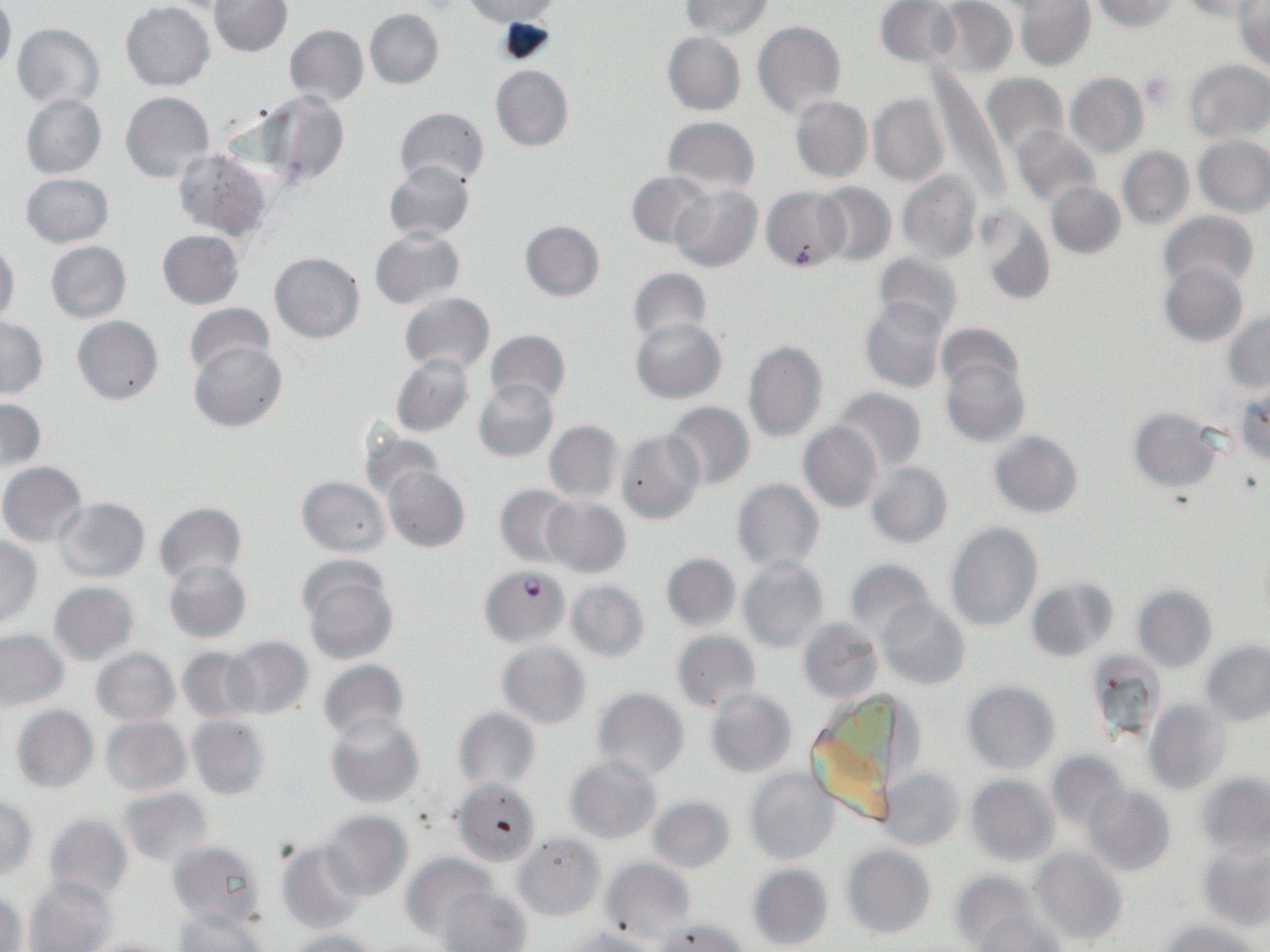
Approximate bounding boxes as [x1, y1, x2, y2] in pixels. Plasmodium falciparum-infected red blood cell locations: [481, 564, 568, 645]. Platelet locations: [1140, 72, 1174, 109]. Uninfected red blood cell locations: [0, 0, 15, 73], [931, 0, 1016, 79], [1090, 0, 1177, 32], [211, 1, 291, 57], [465, 1, 561, 24], [681, 1, 771, 39], [875, 1, 960, 67], [1017, 1, 1094, 69], [1178, 1, 1259, 20], [1233, 2, 1270, 70], [122, 3, 214, 90], [365, 8, 444, 89], [753, 19, 845, 120], [12, 24, 106, 108], [284, 25, 368, 106], [662, 32, 745, 115], [1184, 60, 1269, 142], [490, 65, 573, 152], [929, 67, 1001, 196], [983, 73, 1067, 160], [1066, 73, 1148, 158], [120, 91, 214, 182], [260, 92, 348, 186], [21, 93, 106, 179], [869, 93, 949, 186], [790, 96, 871, 182], [393, 107, 489, 190], [662, 117, 759, 195], [1010, 126, 1099, 208], [1194, 137, 1270, 216], [1121, 142, 1265, 219], [1118, 147, 1193, 229], [172, 149, 274, 241], [383, 160, 474, 244], [31, 170, 122, 325], [898, 170, 983, 264], [626, 171, 711, 251], [20, 174, 113, 247], [812, 182, 896, 267], [1047, 182, 1125, 258], [670, 186, 762, 272], [762, 186, 848, 272], [977, 208, 1053, 306], [1158, 212, 1258, 291], [519, 220, 605, 302], [370, 229, 464, 311], [158, 230, 244, 310], [0, 241, 20, 326], [45, 241, 132, 323], [270, 252, 364, 343], [873, 253, 963, 336], [1160, 261, 1247, 346], [628, 268, 711, 345], [400, 292, 494, 375], [860, 299, 947, 393], [185, 303, 275, 379], [1223, 313, 1270, 393], [72, 316, 164, 404], [631, 317, 726, 403], [0, 319, 48, 397], [936, 322, 1023, 397], [485, 329, 570, 410], [742, 339, 828, 442], [189, 342, 287, 433], [391, 353, 474, 437], [941, 358, 1029, 448], [473, 378, 558, 462], [1233, 384, 1270, 466], [833, 388, 925, 473], [1, 398, 45, 472], [664, 402, 754, 487], [1128, 407, 1225, 493], [545, 420, 623, 502], [799, 422, 882, 512], [357, 429, 446, 503], [616, 430, 705, 526], [989, 431, 1082, 517], [864, 461, 953, 549], [0, 463, 87, 546], [383, 465, 469, 551], [296, 476, 389, 556], [733, 479, 823, 572], [496, 485, 578, 567], [542, 497, 630, 577], [55, 498, 150, 581], [155, 501, 246, 585], [946, 522, 1042, 631], [0, 536, 41, 626], [662, 554, 740, 632], [738, 557, 828, 655], [165, 559, 251, 643], [844, 559, 935, 642], [299, 564, 398, 664], [1026, 579, 1119, 662], [566, 580, 649, 662], [49, 582, 139, 665], [1133, 585, 1217, 672], [879, 600, 969, 690], [798, 617, 884, 704], [0, 628, 69, 711], [673, 631, 761, 712], [224, 637, 314, 719], [1201, 641, 1270, 726], [498, 642, 590, 729], [178, 647, 259, 723], [92, 648, 178, 724], [1086, 650, 1167, 743], [318, 658, 408, 738], [962, 681, 1060, 774], [592, 687, 688, 782], [705, 689, 797, 778], [804, 695, 907, 830], [1145, 699, 1230, 795], [12, 705, 98, 793], [453, 708, 540, 793], [325, 712, 425, 807], [101, 716, 192, 797], [187, 716, 271, 799], [1045, 751, 1129, 832], [564, 755, 662, 843], [744, 767, 839, 865], [882, 767, 964, 851], [1198, 772, 1270, 858], [966, 774, 1060, 865], [452, 779, 536, 865], [1083, 785, 1175, 876], [116, 788, 212, 865], [0, 795, 38, 880], [647, 795, 734, 874], [321, 812, 413, 900], [44, 814, 132, 904], [514, 832, 605, 920], [167, 840, 268, 927], [1200, 842, 1270, 929], [278, 843, 368, 934], [842, 844, 935, 940], [1031, 847, 1128, 948], [402, 850, 494, 942], [601, 857, 695, 948], [747, 863, 833, 951], [950, 870, 1040, 946], [26, 877, 114, 951], [439, 885, 531, 952], [1, 888, 26, 950], [172, 907, 269, 952], [976, 910, 1066, 952], [654, 916, 751, 952], [1160, 920, 1261, 952], [562, 927, 662, 952], [278, 929, 381, 952], [84, 936, 179, 952]. Slide-level diagnosis: Plasmodium falciparum. Light microscopy. One field of a larger specimen. 1000x magnification. May-Grünwald-Giemsa stain. Image is 1270×952 pixels. Thin blood smear.